Classify this cell by malaria status.
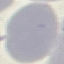

It is uninfected.

{
  "preparation": "thin blood smear",
  "capture": "smartphone through the microscope eyepiece",
  "image_type": "automatically extracted cell patch, resized to 64 × 64 pixels",
  "stain": "Giemsa"
}